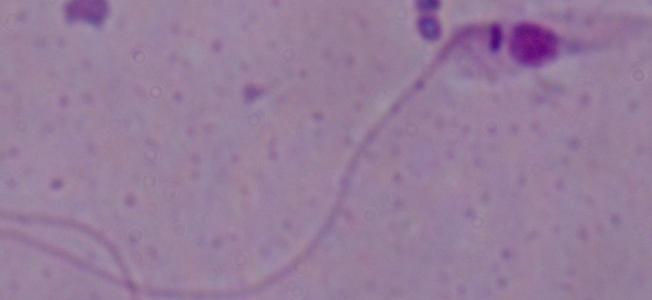

Micrograph. Captured at 1000x magnification. A Leishmania parasite is seen.